State which parasite is depicted.
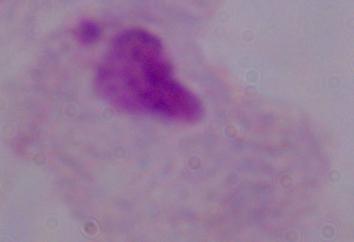
This is a trichomonad.

Captured at 1000x magnification. Micrograph.